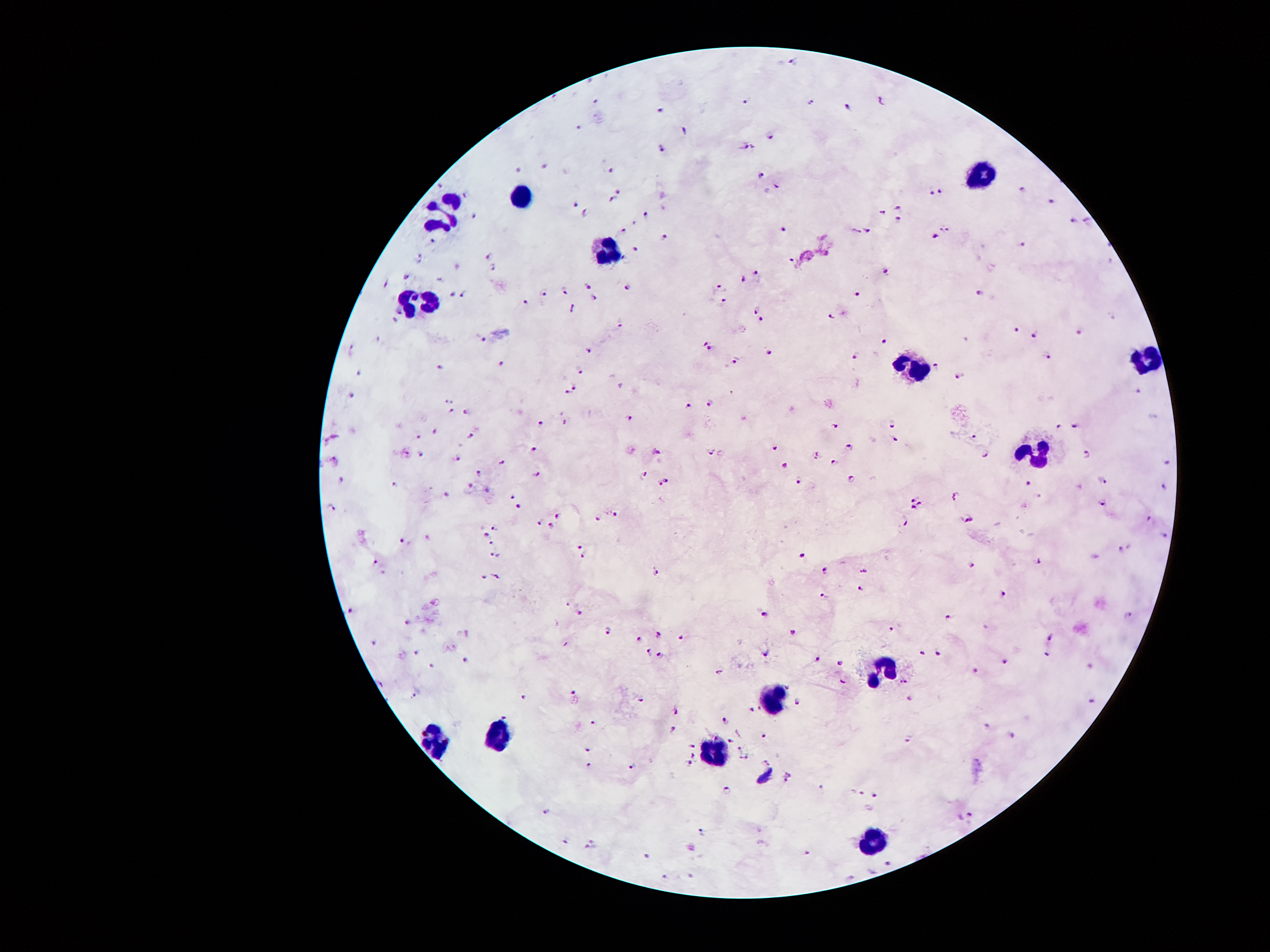

Approximate object centers, in pixels from the top-left corner. Malaria parasite locations: (x=795, y=60), (x=593, y=98), (x=746, y=98), (x=811, y=98), (x=879, y=100), (x=660, y=104), (x=843, y=106), (x=582, y=127), (x=683, y=130), (x=772, y=136), (x=746, y=144), (x=658, y=146), (x=543, y=165), (x=606, y=169), (x=519, y=170), (x=763, y=170), (x=440, y=182), (x=776, y=184), (x=940, y=190), (x=1024, y=190), (x=620, y=191), (x=929, y=193), (x=461, y=195), (x=614, y=197), (x=1053, y=201), (x=576, y=203), (x=900, y=205), (x=587, y=210), (x=883, y=210), (x=645, y=212), (x=473, y=214), (x=898, y=218), (x=1072, y=220), (x=1087, y=220), (x=633, y=222), (x=784, y=226), (x=944, y=226), (x=624, y=228), (x=868, y=228), (x=433, y=239), (x=664, y=239), (x=935, y=239), (x=1024, y=247), (x=637, y=251), (x=488, y=254), (x=421, y=256), (x=792, y=258), (x=456, y=266), (x=494, y=268), (x=887, y=270), (x=755, y=272), (x=406, y=275), (x=744, y=277), (x=438, y=279), (x=627, y=281), (x=389, y=285), (x=719, y=285), (x=589, y=287), (x=564, y=289), (x=452, y=291), (x=461, y=293), (x=543, y=293), (x=977, y=293), (x=855, y=294), (x=595, y=296), (x=723, y=300), (x=522, y=302), (x=398, y=308), (x=572, y=308), (x=755, y=310), (x=830, y=315), (x=396, y=319), (x=763, y=321), (x=620, y=325), (x=1017, y=329), (x=1080, y=329), (x=1032, y=333), (x=480, y=338), (x=708, y=340), (x=885, y=340), (x=351, y=350), (x=589, y=350), (x=771, y=350), (x=853, y=357), (x=1047, y=357), (x=736, y=361), (x=503, y=363), (x=440, y=365), (x=935, y=367), (x=358, y=371), (x=582, y=371), (x=958, y=376), (x=576, y=388), (x=564, y=390), (x=1139, y=390), (x=352, y=392), (x=450, y=397), (x=709, y=397), (x=688, y=403), (x=452, y=411), (x=467, y=411), (x=562, y=420), (x=629, y=420), (x=536, y=422), (x=835, y=426), (x=1078, y=426), (x=891, y=428), (x=1059, y=428), (x=435, y=434), (x=333, y=436), (x=469, y=436), (x=975, y=436), (x=419, y=438), (x=324, y=441), (x=898, y=441), (x=534, y=445), (x=849, y=445), (x=772, y=447), (x=709, y=449), (x=654, y=451), (x=1087, y=451), (x=402, y=453), (x=816, y=453), (x=984, y=453), (x=419, y=455), (x=335, y=459), (x=461, y=459), (x=835, y=459), (x=1168, y=459), (x=501, y=460), (x=782, y=466), (x=478, y=470), (x=536, y=472), (x=646, y=472), (x=851, y=474), (x=339, y=476), (x=666, y=481), (x=795, y=481), (x=469, y=483), (x=660, y=483), (x=1026, y=483), (x=1101, y=483), (x=1168, y=483), (x=396, y=485), (x=488, y=487), (x=956, y=491), (x=448, y=495), (x=513, y=495), (x=1040, y=495), (x=914, y=499), (x=919, y=502), (x=520, y=504), (x=1103, y=506), (x=914, y=508), (x=331, y=510), (x=616, y=512), (x=559, y=514), (x=1149, y=516), (x=593, y=518), (x=969, y=518), (x=540, y=521), (x=904, y=523), (x=553, y=525), (x=494, y=527), (x=488, y=531), (x=1162, y=533), (x=429, y=539), (x=404, y=541), (x=490, y=542), (x=582, y=544), (x=1124, y=548), (x=799, y=550), (x=494, y=554), (x=582, y=554), (x=377, y=562), (x=1038, y=562), (x=973, y=563), (x=824, y=569), (x=862, y=569), (x=656, y=571), (x=496, y=575), (x=480, y=577), (x=860, y=588), (x=824, y=594), (x=1005, y=594), (x=566, y=604), (x=351, y=609), (x=580, y=613), (x=765, y=613), (x=1129, y=613), (x=948, y=617), (x=408, y=621), (x=891, y=626), (x=606, y=630), (x=467, y=632), (x=656, y=632), (x=793, y=632), (x=679, y=636), (x=1051, y=636), (x=637, y=638), (x=375, y=644), (x=415, y=651), (x=767, y=651), (x=919, y=651), (x=937, y=651), (x=646, y=653), (x=660, y=653), (x=1047, y=653), (x=813, y=657), (x=465, y=661), (x=1005, y=661), (x=839, y=665), (x=1091, y=665), (x=433, y=666), (x=975, y=670), (x=719, y=672), (x=843, y=680), (x=902, y=682), (x=379, y=684), (x=414, y=691), (x=524, y=691), (x=572, y=691), (x=910, y=695), (x=641, y=699), (x=799, y=699), (x=1091, y=701), (x=675, y=710), (x=752, y=710), (x=507, y=714), (x=725, y=722), (x=593, y=724), (x=984, y=726), (x=671, y=729), (x=765, y=733), (x=1013, y=737), (x=729, y=739), (x=906, y=739), (x=692, y=743), (x=738, y=747), (x=587, y=750), (x=692, y=756), (x=746, y=756), (x=769, y=760), (x=689, y=762), (x=587, y=766), (x=633, y=766), (x=788, y=777), (x=727, y=789), (x=822, y=791), (x=860, y=794), (x=874, y=794), (x=543, y=810), (x=969, y=813), (x=702, y=832), (x=566, y=842), (x=591, y=844), (x=809, y=850), (x=645, y=855), (x=887, y=861), (x=666, y=876), (x=692, y=876). Leukocyte locations: (x=982, y=171), (x=518, y=196), (x=441, y=207), (x=602, y=251), (x=426, y=298), (x=1147, y=361), (x=916, y=371), (x=1033, y=452), (x=891, y=660), (x=774, y=686), (x=496, y=733), (x=430, y=740), (x=715, y=752), (x=872, y=843). Thick blood smear. Patient malaria status: positive for Plasmodium falciparum. Giemsa-stained preparation. Image is 1270×952 pixels. Smartphone photograph taken through the microscope eyepiece. One field from this slide. 100x magnification.